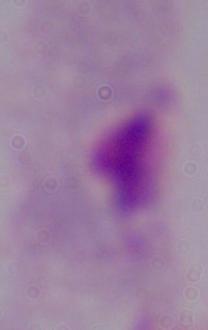

Summary:
  - Modality: micrograph
  - Magnification: 1000x
  - Identification: trichomonad